Name the parasite shown.
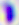
This is Toxoplasma gondii.

Summary:
  - Modality: micrograph
  - Magnification: 400x